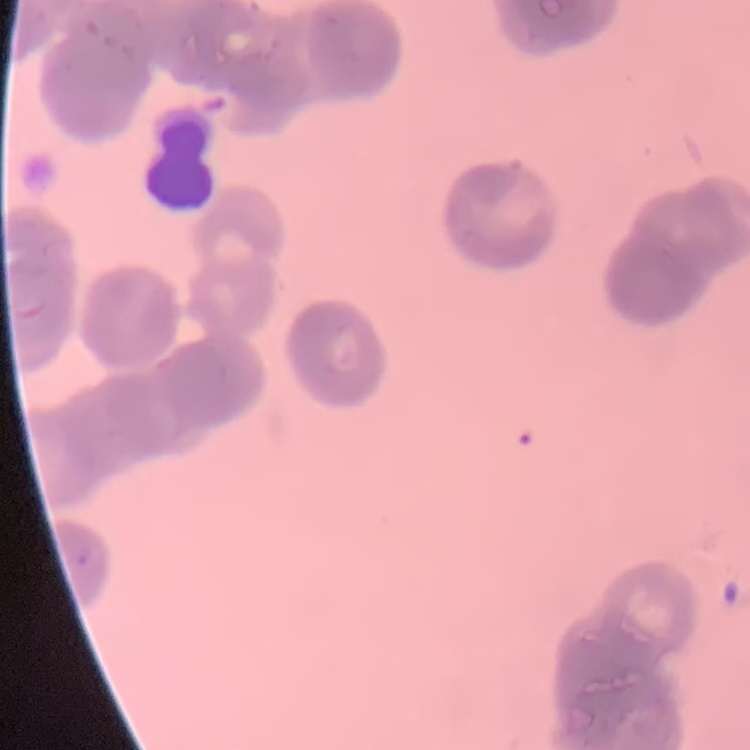

Summary:
  - Erythrocyte morphology: rouleaux formation
  - Stain: Field's or Giemsa
  - Image type: square crop of a larger photomicrograph
  - Preparation: thin peripheral smear